Outline each uninfected red blood cell.
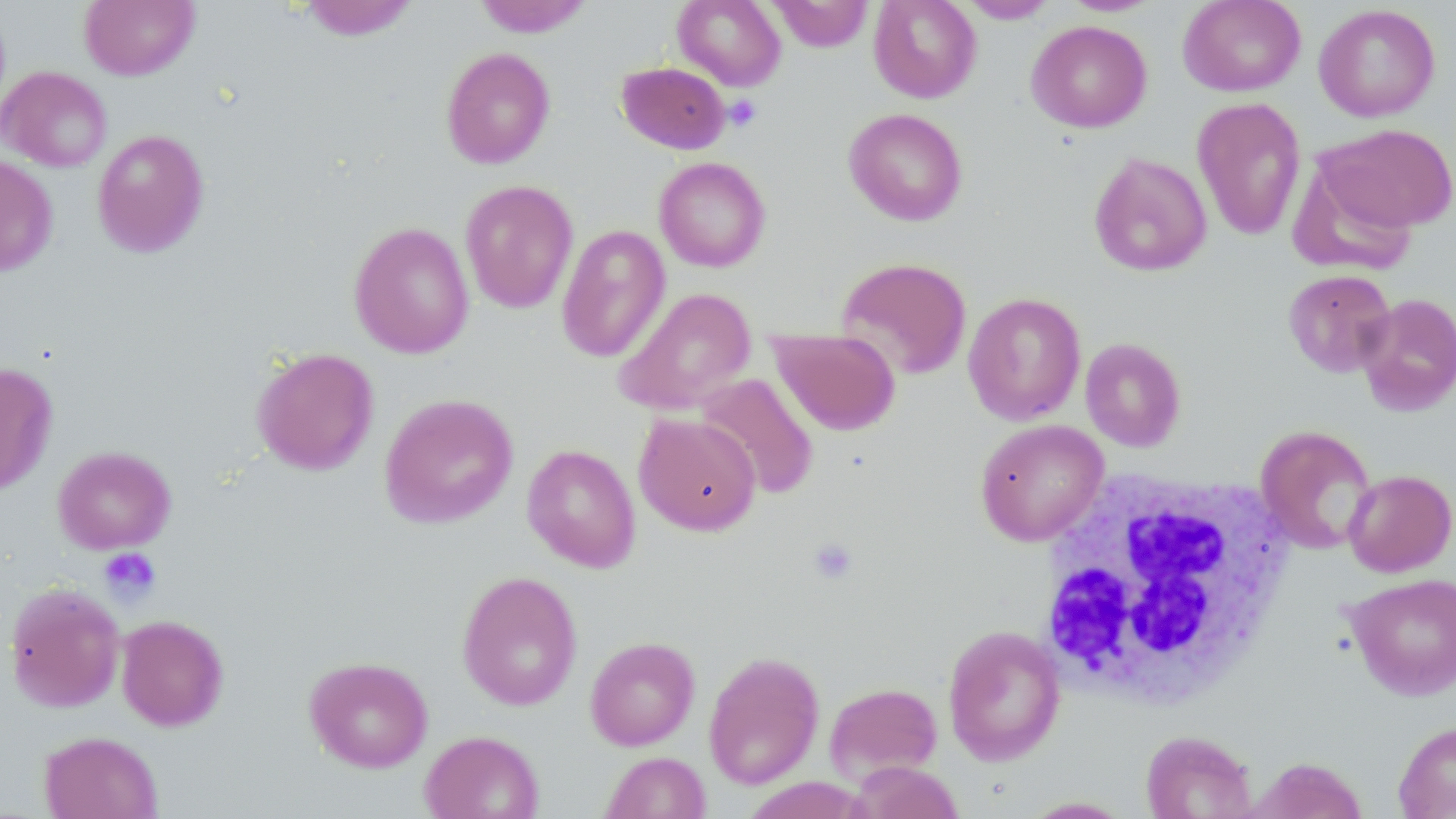
Approximate bounding boxes as [x1, y1, x2, y2] in pixels.
Uninfected red blood cells: [80, 0, 199, 80], [297, 0, 420, 41], [474, 0, 593, 37], [673, 0, 786, 90], [769, 0, 872, 52], [868, 0, 982, 103], [959, 0, 1057, 23], [1177, 0, 1306, 97], [1059, 1, 1163, 16], [1313, 3, 1441, 122], [1026, 20, 1152, 133], [440, 47, 556, 169], [616, 61, 731, 154], [1, 67, 112, 172], [1192, 97, 1306, 240], [843, 108, 968, 225], [1316, 124, 1456, 233], [92, 129, 210, 258], [1089, 152, 1212, 276], [0, 154, 58, 277], [654, 156, 771, 272], [460, 180, 579, 314], [349, 221, 474, 359], [556, 224, 670, 363], [835, 256, 972, 381], [1283, 269, 1396, 378], [613, 287, 756, 415], [963, 292, 1086, 425], [1355, 293, 1456, 414], [768, 328, 902, 436], [1080, 337, 1186, 452], [252, 347, 379, 475], [0, 362, 58, 496], [695, 373, 820, 500], [379, 393, 519, 529], [634, 413, 761, 535], [975, 419, 1108, 545], [1256, 425, 1377, 555], [522, 443, 641, 573], [52, 445, 176, 554], [1343, 468, 1456, 577], [456, 570, 583, 710], [1345, 572, 1456, 701], [5, 582, 125, 713], [116, 614, 229, 731], [942, 625, 1066, 764], [585, 636, 700, 751], [703, 651, 824, 789], [304, 656, 433, 773], [823, 682, 942, 783], [1392, 721, 1456, 818], [420, 730, 544, 819], [1140, 730, 1256, 818], [38, 731, 163, 819], [600, 751, 711, 818], [1251, 756, 1368, 819], [849, 762, 964, 819], [1019, 796, 1136, 818].

slide-level diagnosis = negative for blood parasites
field of view = one of a larger specimen
preparation = thin blood smear
magnification = 1000x
image size = 1456×819 pixels
stain = May-Grünwald-Giemsa
modality = optical microscopy
white blood cell locations = approximate bounding boxes as [x1, y1, x2, y2] in pixels: [1037, 470, 1299, 713]
platelet locations = approximate bounding boxes as [x1, y1, x2, y2] in pixels: [724, 94, 761, 132], [808, 537, 859, 585], [98, 547, 161, 603]